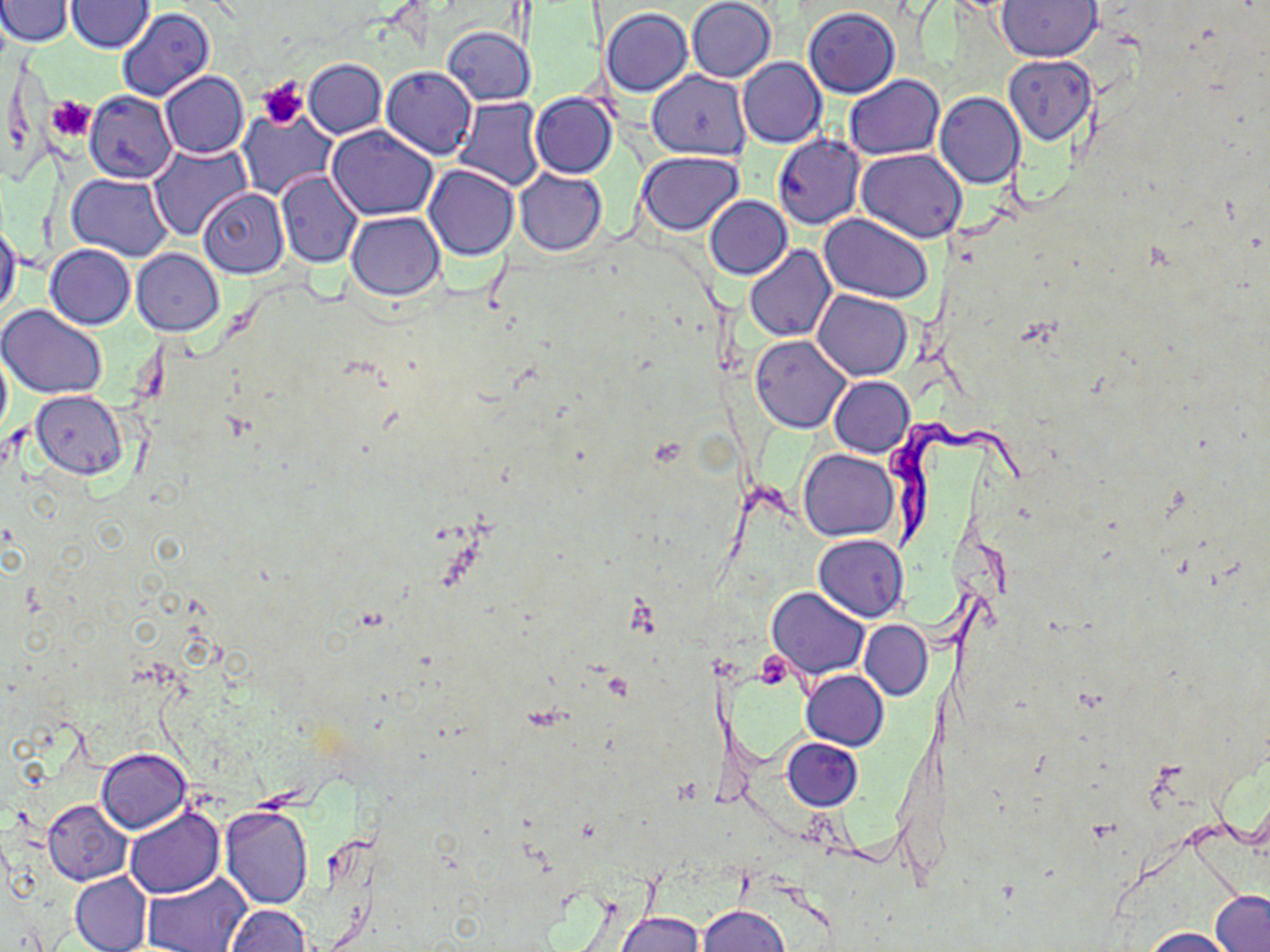

Summary:
  - Coordinate format: approximate bounding boxes as (x1,y1)-(x2,y2) corner pairs in pixels
  - Platelet locations: (259,78)-(308,129), (47,97)-(94,141), (754,650)-(794,689)
  - Trypanosoma brucei locations: (883,417)-(1026,555)
  - Uninfected red blood cell locations: (0,0)-(72,47), (686,0)-(777,82), (65,1)-(154,54), (997,1)-(1101,61), (116,7)-(215,102), (601,8)-(692,96), (803,8)-(901,98), (441,26)-(535,105), (1003,54)-(1097,145), (737,57)-(826,148), (303,58)-(386,139), (382,66)-(477,160), (647,70)-(750,159), (159,71)-(248,159), (844,75)-(945,161), (85,91)-(178,183), (935,91)-(1026,189), (530,92)-(618,178), (452,97)-(545,192), (237,109)-(336,200), (326,124)-(438,220), (772,133)-(865,229), (147,143)-(252,243), (857,149)-(967,244), (637,152)-(744,234), (424,164)-(519,261), (514,168)-(607,256), (275,170)-(363,268), (68,172)-(174,261), (197,187)-(288,279), (705,196)-(791,279), (347,211)-(445,299), (820,213)-(933,303), (0,217)-(22,319), (25,245)-(125,390), (46,245)-(135,329), (743,245)-(835,342), (132,248)-(224,336), (814,290)-(911,381), (2,306)-(107,400), (751,336)-(852,434), (0,347)-(11,444), (828,376)-(914,458), (30,390)-(129,478), (800,450)-(898,541), (814,533)-(908,622), (767,586)-(869,679), (859,621)-(933,700), (801,670)-(889,750), (782,738)-(862,810), (96,748)-(193,833), (43,798)-(133,885), (124,807)-(224,899), (219,807)-(314,910), (69,871)-(152,952), (142,872)-(252,952), (1210,889)-(1270,952), (225,904)-(311,952), (700,904)-(789,952), (615,912)-(702,952), (1136,926)-(1241,951)
  - Slide-level diagnosis: Trypanosoma brucei
  - Modality: light microscopy
  - Image size: 1270×952 pixels
  - Stain: May-Grünwald-Giemsa
  - Preparation: thin blood smear
  - Magnification: 1000x
  - Field of view: one of a larger specimen